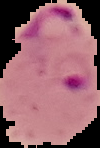 Cell region segmented out of the field of view; the surrounding area is masked to black. From a thin blood film. Result: Plasmodium parasites detected. Image is 100×148 pixels.